Give the extent of all Plasmodium falciparum-infected red blood cells.
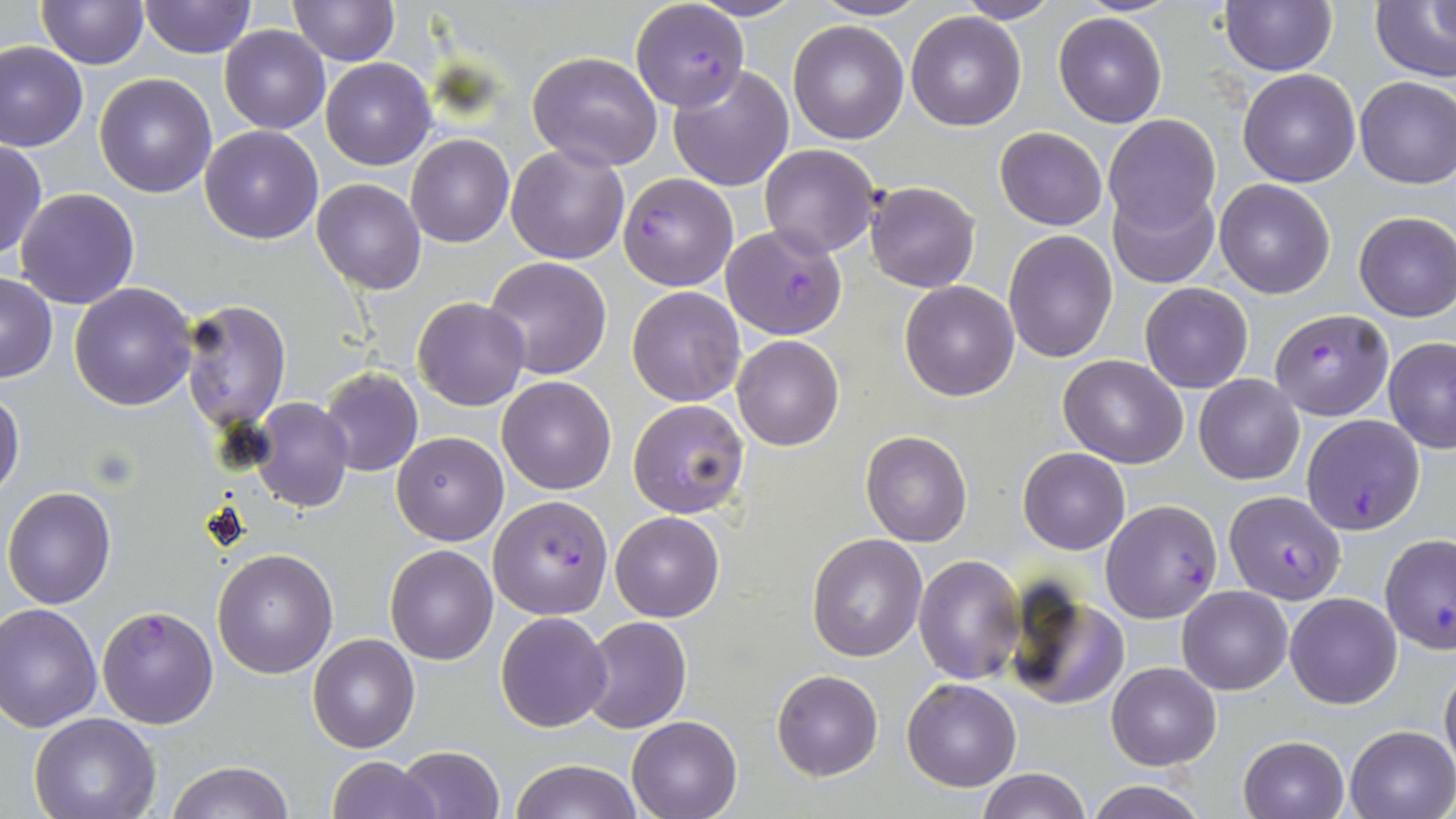

Approximate bounding boxes as (x1, y1, x2, y2) in pixels.
Plasmodium falciparum-infected red blood cells: (631, 2, 750, 111), (619, 173, 737, 291), (722, 224, 848, 340), (1269, 308, 1394, 420), (1300, 414, 1426, 534), (1225, 489, 1345, 603), (488, 495, 612, 619), (1100, 498, 1223, 624), (96, 605, 218, 730).

Summary:
  - Uninfected red blood cell locations: (37, 0, 147, 69), (138, 0, 255, 58), (287, 0, 398, 66), (687, 0, 804, 20), (812, 0, 929, 21), (954, 0, 1060, 24), (1220, 0, 1338, 76), (1372, 1, 1456, 85), (1428, 1, 1456, 46), (906, 10, 1027, 130), (1053, 11, 1168, 127), (787, 20, 909, 145), (220, 26, 329, 135), (0, 39, 90, 152), (527, 52, 663, 171), (321, 58, 434, 169), (667, 64, 794, 190), (1238, 68, 1362, 187), (93, 72, 217, 197), (1354, 76, 1456, 188), (1103, 114, 1219, 235), (199, 125, 324, 244), (995, 127, 1106, 230), (405, 134, 514, 248), (0, 139, 45, 261), (505, 143, 631, 265), (759, 144, 880, 258), (312, 178, 426, 294), (1214, 178, 1336, 298), (864, 180, 980, 293), (1105, 187, 1219, 290), (14, 188, 139, 309), (1353, 211, 1456, 321), (1003, 227, 1119, 363), (484, 256, 613, 380), (0, 273, 57, 383), (898, 279, 1020, 402), (69, 282, 198, 410), (1139, 282, 1254, 393), (626, 286, 746, 406), (412, 296, 530, 411), (178, 299, 290, 429), (731, 334, 844, 451), (1382, 338, 1456, 453), (1058, 355, 1188, 468), (319, 367, 422, 477), (1193, 374, 1305, 485), (495, 375, 617, 494), (0, 387, 25, 499), (248, 397, 354, 512), (628, 398, 749, 517), (860, 428, 974, 547), (391, 431, 508, 545), (1019, 447, 1130, 555), (3, 486, 117, 608), (610, 510, 725, 622), (806, 533, 928, 662), (1380, 534, 1456, 656), (385, 543, 498, 665), (212, 548, 339, 679), (915, 553, 1026, 685), (1005, 585, 1129, 710), (1176, 586, 1292, 695), (1285, 591, 1402, 708), (0, 603, 101, 731), (495, 611, 613, 731), (579, 616, 692, 733), (308, 633, 421, 752), (1439, 659, 1456, 775), (1105, 661, 1221, 769), (773, 669, 884, 779), (902, 678, 1021, 791), (30, 712, 160, 819), (627, 715, 742, 819), (1345, 726, 1456, 818), (1238, 734, 1348, 818), (394, 745, 506, 819), (327, 755, 440, 819), (508, 758, 645, 818), (166, 760, 293, 819), (977, 768, 1091, 819), (1084, 779, 1211, 819)
  - Slide-level diagnosis: Plasmodium falciparum
  - Field of view: single
  - Modality: optical microscopy
  - Image size: 1456×819 pixels
  - Magnification: 1000x
  - Stain: May-Grünwald-Giemsa
  - Preparation: thin blood smear